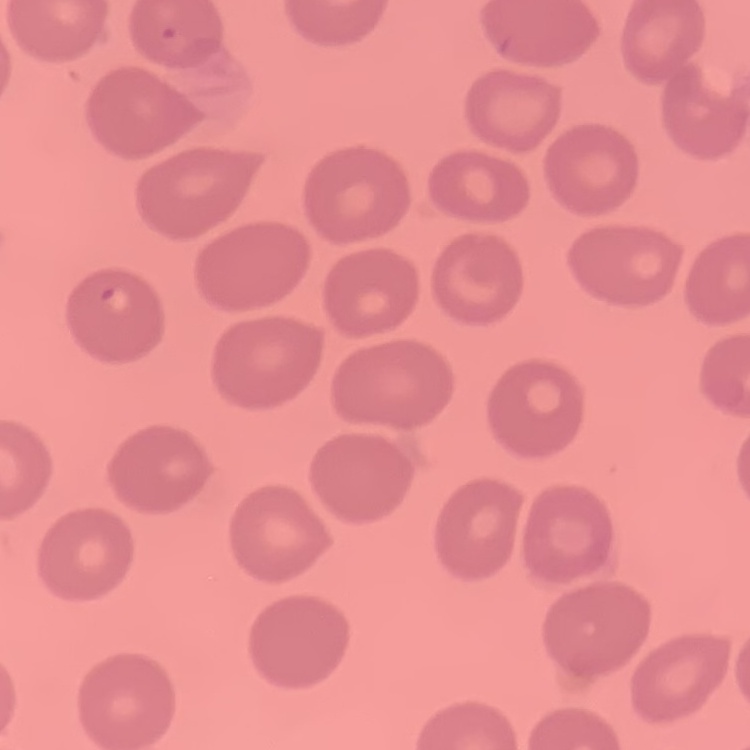

Summary:
  - Erythrocyte morphology: no rouleaux formation
  - Image type: square crop of a larger photomicrograph
  - Preparation: thin blood film
  - Stain: Field's or Giemsa